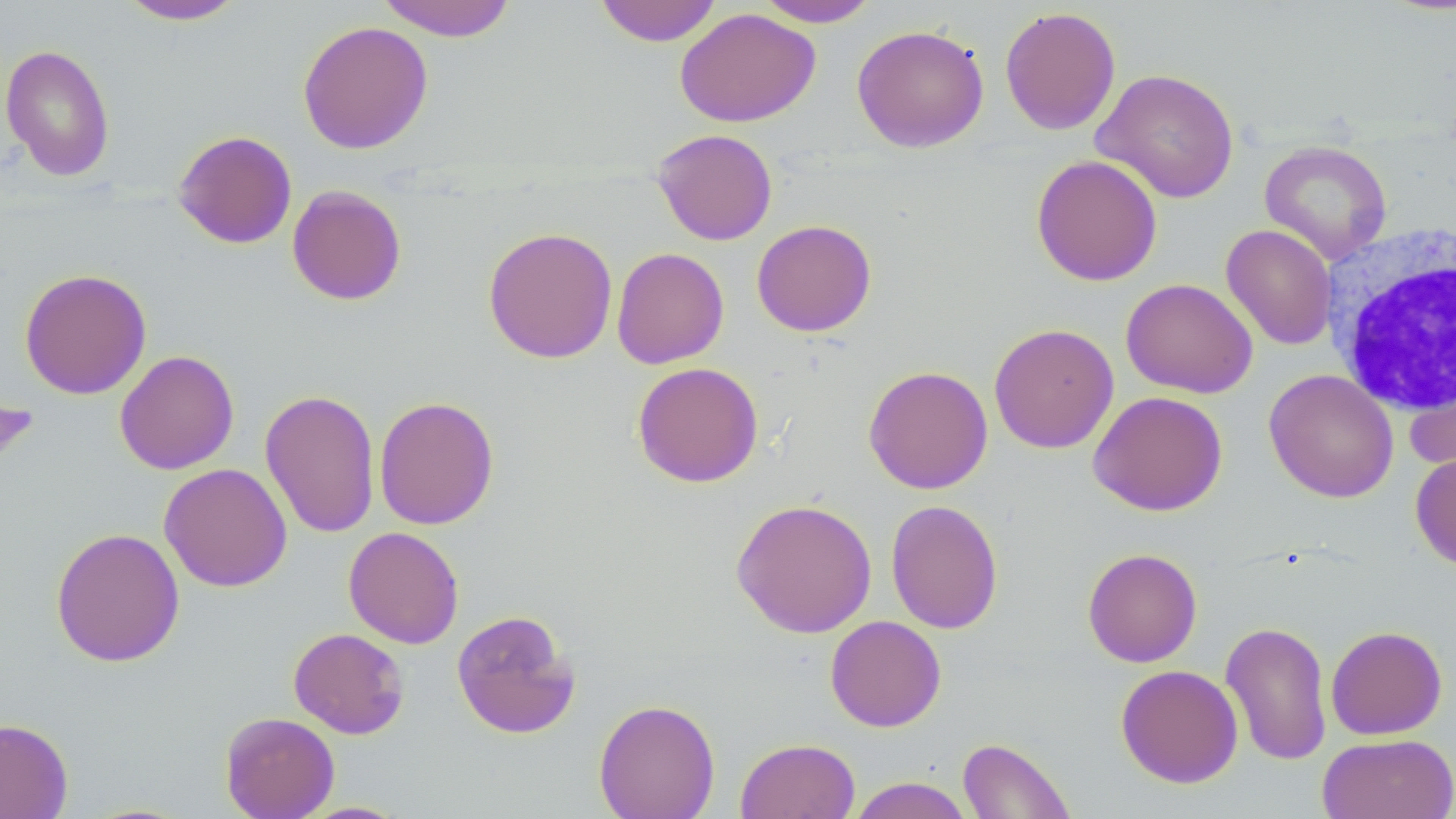 Approximate bounding boxes as named x1/y1/x2/y2 corners in pixels. Uninfected red blood cell locations: (x1=115, y1=0, x2=250, y2=26), (x1=375, y1=0, x2=518, y2=41), (x1=593, y1=0, x2=723, y2=46), (x1=754, y1=0, x2=881, y2=27), (x1=999, y1=6, x2=1121, y2=135), (x1=674, y1=7, x2=821, y2=128), (x1=297, y1=20, x2=433, y2=155), (x1=851, y1=24, x2=989, y2=153), (x1=0, y1=43, x2=116, y2=182), (x1=1092, y1=67, x2=1239, y2=204), (x1=652, y1=128, x2=778, y2=245), (x1=172, y1=130, x2=298, y2=249), (x1=1259, y1=140, x2=1392, y2=265), (x1=1031, y1=154, x2=1162, y2=287), (x1=286, y1=185, x2=407, y2=306), (x1=751, y1=219, x2=876, y2=337), (x1=1221, y1=224, x2=1337, y2=350), (x1=482, y1=226, x2=618, y2=364), (x1=611, y1=247, x2=729, y2=369), (x1=19, y1=267, x2=152, y2=400), (x1=1120, y1=277, x2=1258, y2=398), (x1=988, y1=323, x2=1119, y2=454), (x1=115, y1=350, x2=239, y2=475), (x1=632, y1=362, x2=764, y2=488), (x1=863, y1=365, x2=993, y2=494), (x1=1406, y1=367, x2=1456, y2=477), (x1=1263, y1=369, x2=1399, y2=503), (x1=260, y1=388, x2=381, y2=539), (x1=1088, y1=391, x2=1228, y2=516), (x1=374, y1=395, x2=500, y2=530), (x1=1410, y1=451, x2=1456, y2=570), (x1=159, y1=463, x2=292, y2=592), (x1=731, y1=498, x2=877, y2=638), (x1=885, y1=499, x2=1004, y2=634), (x1=343, y1=526, x2=465, y2=649), (x1=50, y1=527, x2=185, y2=667), (x1=1082, y1=548, x2=1203, y2=668), (x1=451, y1=609, x2=581, y2=739), (x1=825, y1=615, x2=947, y2=732), (x1=1221, y1=620, x2=1333, y2=767), (x1=1325, y1=625, x2=1448, y2=740), (x1=288, y1=627, x2=410, y2=739), (x1=1115, y1=664, x2=1243, y2=788), (x1=594, y1=698, x2=720, y2=819), (x1=220, y1=711, x2=339, y2=819), (x1=0, y1=717, x2=73, y2=819), (x1=1317, y1=733, x2=1456, y2=819), (x1=957, y1=737, x2=1075, y2=819), (x1=735, y1=738, x2=860, y2=819), (x1=847, y1=777, x2=975, y2=818), (x1=295, y1=801, x2=411, y2=818). White blood cell locations: (x1=1322, y1=226, x2=1455, y2=417). Slide-level diagnosis: no evidence of blood parasites. May-Grünwald-Giemsa-stained preparation. Thin blood smear. Captured at 1000x magnification. Image is 1456×819 pixels. Single field of view. Optical microscopy.